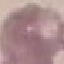
Summary:
  - Malaria status: uninfected
  - Preparation: thin blood film
  - Capture: smartphone through the microscope eyepiece
  - Stain: Giemsa
  - Image type: cell patch, automatically extracted from a larger field of view and resized to 64 × 64 pixels